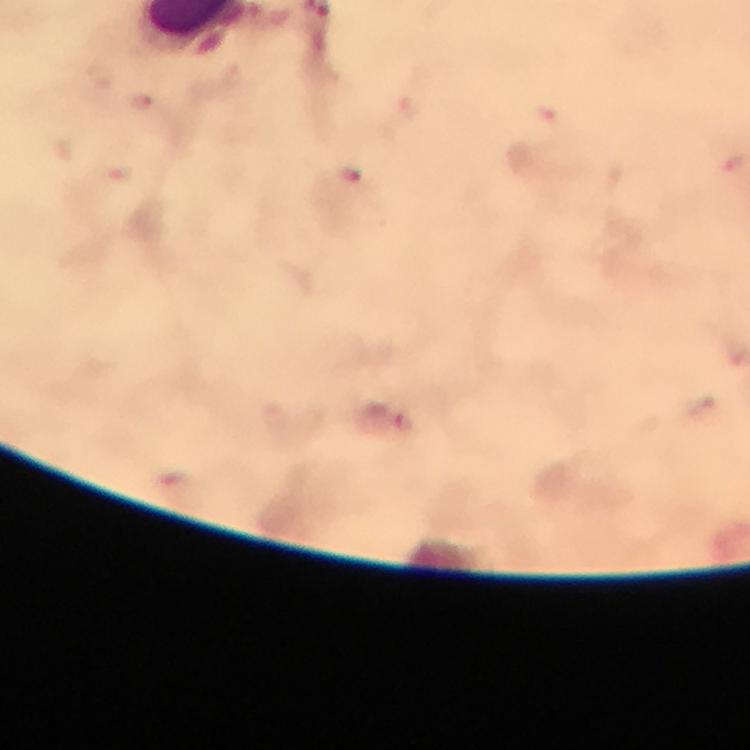

malaria parasite locations = approximate centers as [x, y] in pixels: [733, 163], [353, 177], [405, 423]
magnification = 100x
image size = 750×750 pixels
capture = smartphone mounted on the microscope
context = from a diagnostic examination for malaria
stain = Giemsa
immersion oil = applied
preparation = thick blood film
cropped from = a single field of view